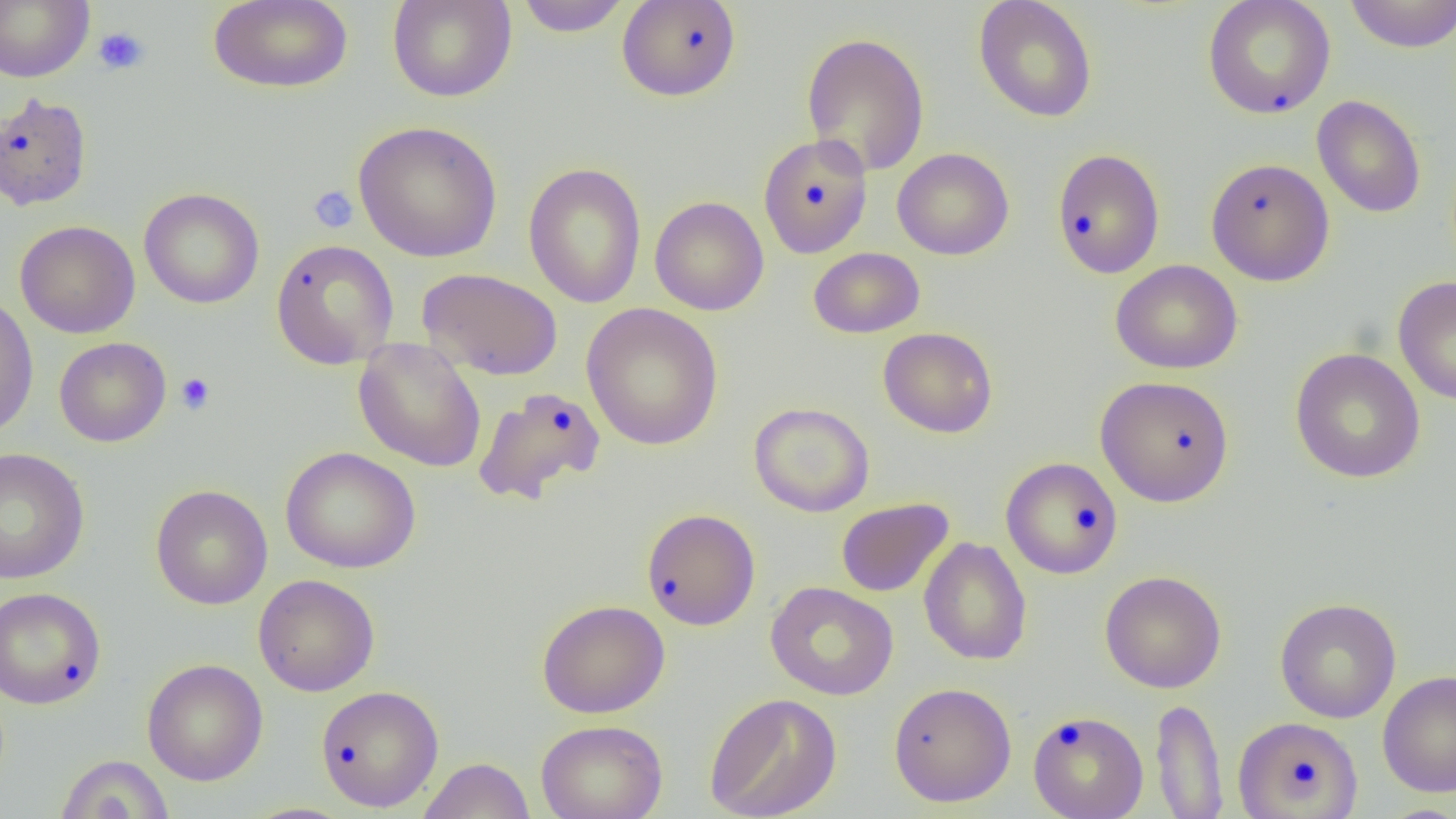
Approximate bounding boxes as named x1/y1/x2/y2 corners in pixels. Platelet locations: (x1=93, y1=26, x2=150, y2=76), (x1=308, y1=185, x2=359, y2=233), (x1=175, y1=372, x2=215, y2=414). Uninfected red blood cell locations: (x1=0, y1=0, x2=94, y2=83), (x1=209, y1=0, x2=353, y2=93), (x1=387, y1=0, x2=517, y2=102), (x1=515, y1=0, x2=631, y2=37), (x1=616, y1=0, x2=742, y2=102), (x1=1343, y1=0, x2=1456, y2=52), (x1=973, y1=1, x2=1098, y2=123), (x1=1202, y1=1, x2=1336, y2=119), (x1=801, y1=31, x2=930, y2=177), (x1=0, y1=91, x2=93, y2=211), (x1=1312, y1=94, x2=1426, y2=219), (x1=353, y1=120, x2=503, y2=263), (x1=757, y1=134, x2=873, y2=259), (x1=892, y1=147, x2=1015, y2=260), (x1=1051, y1=148, x2=1165, y2=279), (x1=1205, y1=157, x2=1335, y2=286), (x1=523, y1=161, x2=647, y2=308), (x1=138, y1=187, x2=265, y2=309), (x1=650, y1=196, x2=769, y2=315), (x1=14, y1=220, x2=140, y2=339), (x1=270, y1=239, x2=399, y2=369), (x1=809, y1=247, x2=924, y2=338), (x1=1112, y1=260, x2=1242, y2=374), (x1=417, y1=267, x2=562, y2=380), (x1=1393, y1=276, x2=1456, y2=405), (x1=0, y1=293, x2=38, y2=439), (x1=581, y1=303, x2=724, y2=451), (x1=878, y1=327, x2=998, y2=438), (x1=54, y1=337, x2=171, y2=447), (x1=353, y1=337, x2=487, y2=472), (x1=1289, y1=347, x2=1426, y2=484), (x1=1095, y1=375, x2=1234, y2=507), (x1=472, y1=386, x2=606, y2=506), (x1=749, y1=401, x2=875, y2=517), (x1=280, y1=446, x2=421, y2=573), (x1=0, y1=447, x2=90, y2=584), (x1=1000, y1=456, x2=1123, y2=579), (x1=150, y1=484, x2=273, y2=610), (x1=836, y1=498, x2=953, y2=597), (x1=641, y1=508, x2=761, y2=630), (x1=918, y1=537, x2=1032, y2=665), (x1=1100, y1=570, x2=1227, y2=693), (x1=253, y1=574, x2=380, y2=696), (x1=765, y1=582, x2=899, y2=701), (x1=0, y1=586, x2=106, y2=709), (x1=1274, y1=597, x2=1402, y2=723), (x1=537, y1=599, x2=670, y2=719), (x1=142, y1=658, x2=268, y2=785), (x1=1377, y1=670, x2=1456, y2=797), (x1=888, y1=682, x2=1017, y2=807), (x1=316, y1=685, x2=445, y2=812), (x1=704, y1=692, x2=842, y2=819), (x1=1151, y1=697, x2=1228, y2=818), (x1=1028, y1=710, x2=1149, y2=819), (x1=1233, y1=716, x2=1363, y2=819), (x1=536, y1=719, x2=667, y2=819), (x1=55, y1=754, x2=174, y2=818), (x1=418, y1=757, x2=536, y2=819), (x1=238, y1=803, x2=360, y2=819). Slide-level diagnosis: no evidence of blood parasites. Single field of view. Captured at 1000x magnification. Thin blood smear. Optical microscopy. Image is 1456×819 pixels.